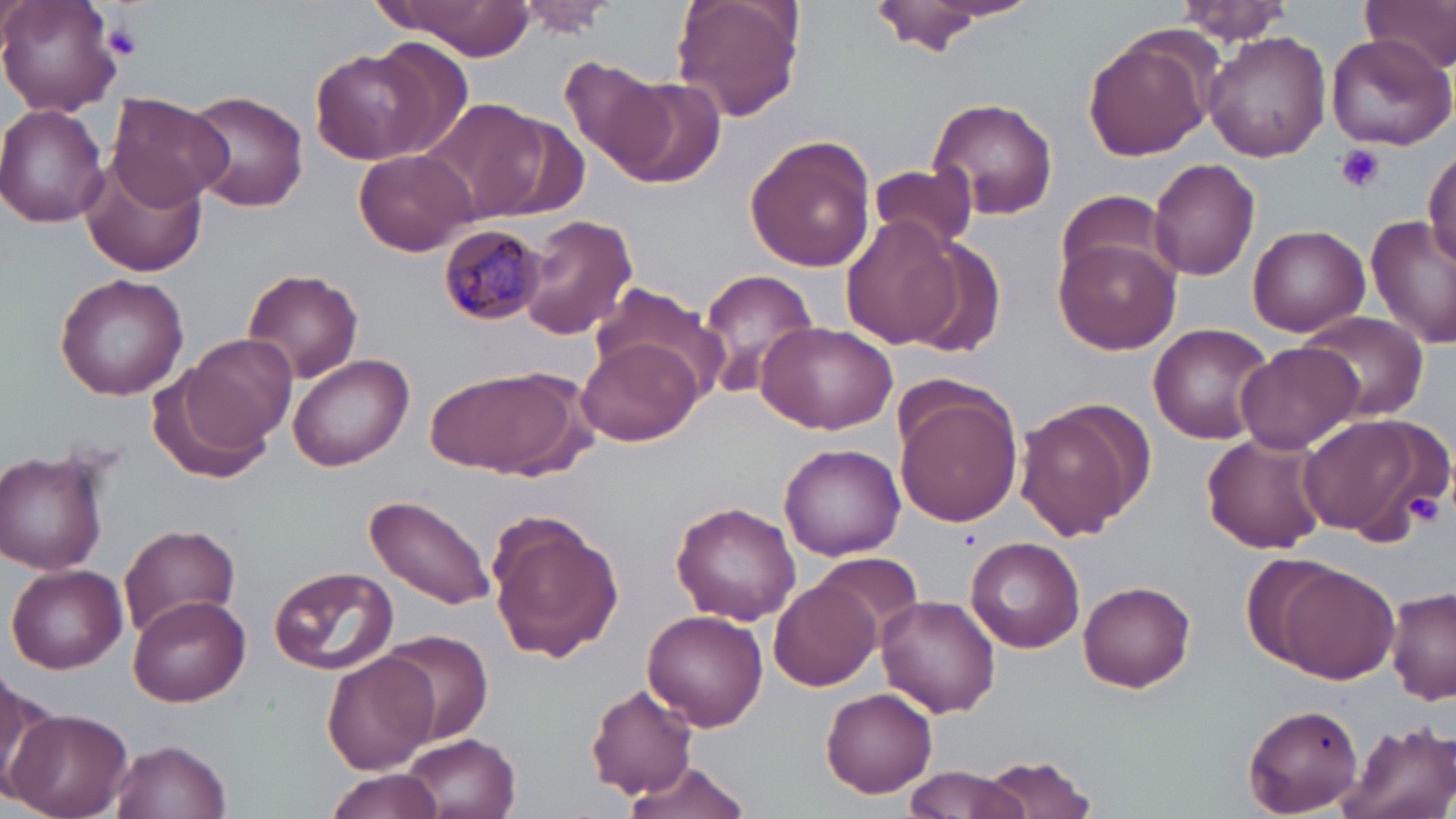
Approximate bounding boxes as named x1/y1/x2/y2 corners in pixels. Plasmodium malariae-infected red blood cell locations: (x1=438, y1=224, x2=547, y2=327). Platelet locations: (x1=106, y1=22, x2=143, y2=59), (x1=1333, y1=145, x2=1386, y2=195), (x1=1399, y1=490, x2=1445, y2=530). Uninfected red blood cell locations: (x1=1, y1=0, x2=123, y2=116), (x1=375, y1=0, x2=536, y2=58), (x1=670, y1=0, x2=806, y2=122), (x1=864, y1=0, x2=1010, y2=56), (x1=1362, y1=0, x2=1456, y2=72), (x1=509, y1=1, x2=622, y2=36), (x1=1170, y1=1, x2=1297, y2=43), (x1=1203, y1=29, x2=1332, y2=161), (x1=1082, y1=30, x2=1219, y2=162), (x1=1326, y1=31, x2=1456, y2=151), (x1=370, y1=34, x2=473, y2=156), (x1=309, y1=48, x2=441, y2=165), (x1=559, y1=56, x2=666, y2=171), (x1=611, y1=75, x2=727, y2=189), (x1=185, y1=90, x2=310, y2=211), (x1=105, y1=93, x2=231, y2=210), (x1=924, y1=95, x2=1059, y2=221), (x1=421, y1=98, x2=552, y2=223), (x1=0, y1=104, x2=114, y2=227), (x1=744, y1=134, x2=876, y2=271), (x1=1425, y1=147, x2=1456, y2=272), (x1=352, y1=148, x2=477, y2=255), (x1=78, y1=156, x2=209, y2=278), (x1=1147, y1=159, x2=1261, y2=281), (x1=866, y1=163, x2=978, y2=251), (x1=1052, y1=192, x2=1181, y2=294), (x1=515, y1=212, x2=638, y2=342), (x1=1365, y1=214, x2=1456, y2=348), (x1=840, y1=215, x2=964, y2=352), (x1=1247, y1=224, x2=1370, y2=336), (x1=901, y1=236, x2=1007, y2=357), (x1=1055, y1=236, x2=1183, y2=354), (x1=243, y1=267, x2=365, y2=383), (x1=694, y1=268, x2=819, y2=400), (x1=53, y1=274, x2=189, y2=400), (x1=589, y1=286, x2=732, y2=401), (x1=1294, y1=309, x2=1432, y2=423), (x1=755, y1=318, x2=897, y2=434), (x1=1147, y1=323, x2=1276, y2=444), (x1=180, y1=332, x2=297, y2=450), (x1=578, y1=339, x2=702, y2=447), (x1=1234, y1=341, x2=1367, y2=454), (x1=288, y1=352, x2=415, y2=470), (x1=428, y1=363, x2=591, y2=482), (x1=148, y1=372, x2=272, y2=485), (x1=895, y1=392, x2=1022, y2=526), (x1=1017, y1=402, x2=1146, y2=538), (x1=1297, y1=413, x2=1439, y2=540), (x1=1201, y1=432, x2=1327, y2=555), (x1=779, y1=443, x2=906, y2=559), (x1=1, y1=449, x2=110, y2=575), (x1=365, y1=494, x2=497, y2=613), (x1=670, y1=500, x2=802, y2=626), (x1=485, y1=512, x2=625, y2=662), (x1=120, y1=522, x2=240, y2=638), (x1=965, y1=536, x2=1086, y2=653), (x1=810, y1=550, x2=926, y2=643), (x1=8, y1=563, x2=127, y2=673), (x1=269, y1=564, x2=399, y2=676), (x1=1274, y1=564, x2=1400, y2=681), (x1=770, y1=577, x2=883, y2=692), (x1=1078, y1=580, x2=1196, y2=692), (x1=1385, y1=586, x2=1456, y2=705), (x1=128, y1=595, x2=251, y2=707), (x1=877, y1=595, x2=1001, y2=716), (x1=643, y1=608, x2=765, y2=732), (x1=379, y1=629, x2=496, y2=744), (x1=320, y1=648, x2=438, y2=774), (x1=0, y1=675, x2=58, y2=802), (x1=588, y1=684, x2=697, y2=797), (x1=820, y1=686, x2=938, y2=799), (x1=1243, y1=702, x2=1366, y2=816), (x1=8, y1=709, x2=132, y2=819), (x1=1335, y1=719, x2=1456, y2=819), (x1=403, y1=731, x2=520, y2=818), (x1=110, y1=737, x2=233, y2=819), (x1=981, y1=754, x2=1101, y2=818), (x1=621, y1=757, x2=756, y2=819), (x1=901, y1=765, x2=1030, y2=819), (x1=322, y1=769, x2=446, y2=819). Slide-level diagnosis: Plasmodium malariae. Thin blood film. 1000x magnification. One field of a larger specimen. May-Grünwald-Giemsa-stained preparation. Optical microscopy. Image is 1456×819 pixels.